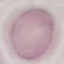

Summary:
  - Malaria status: uninfected
  - Capture: smartphone camera at the microscope eyepiece
  - Image type: automatically extracted cell patch, resized to 64 × 64 pixels
  - Stain: Giemsa
  - Preparation: thin smear